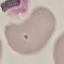
Malaria status: uninfected. Automatically extracted cell patch, resized to 64 × 64 pixels. Photographed with a smartphone camera at the microscope eyepiece. Thin blood film. Giemsa-stained preparation.